Assess this cell for malaria.
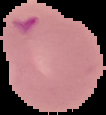
Parasitized.

{
  "preparation": "thin blood smear",
  "image_size": "106×115 pixels",
  "image_type": "segmented cell region on a black background"
}